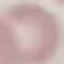
malaria status = uninfected
stain = Giemsa
capture = smartphone camera at the microscope eyepiece
preparation = thin blood film
image type = automatically extracted cell patch, resized to 64 × 64 pixels